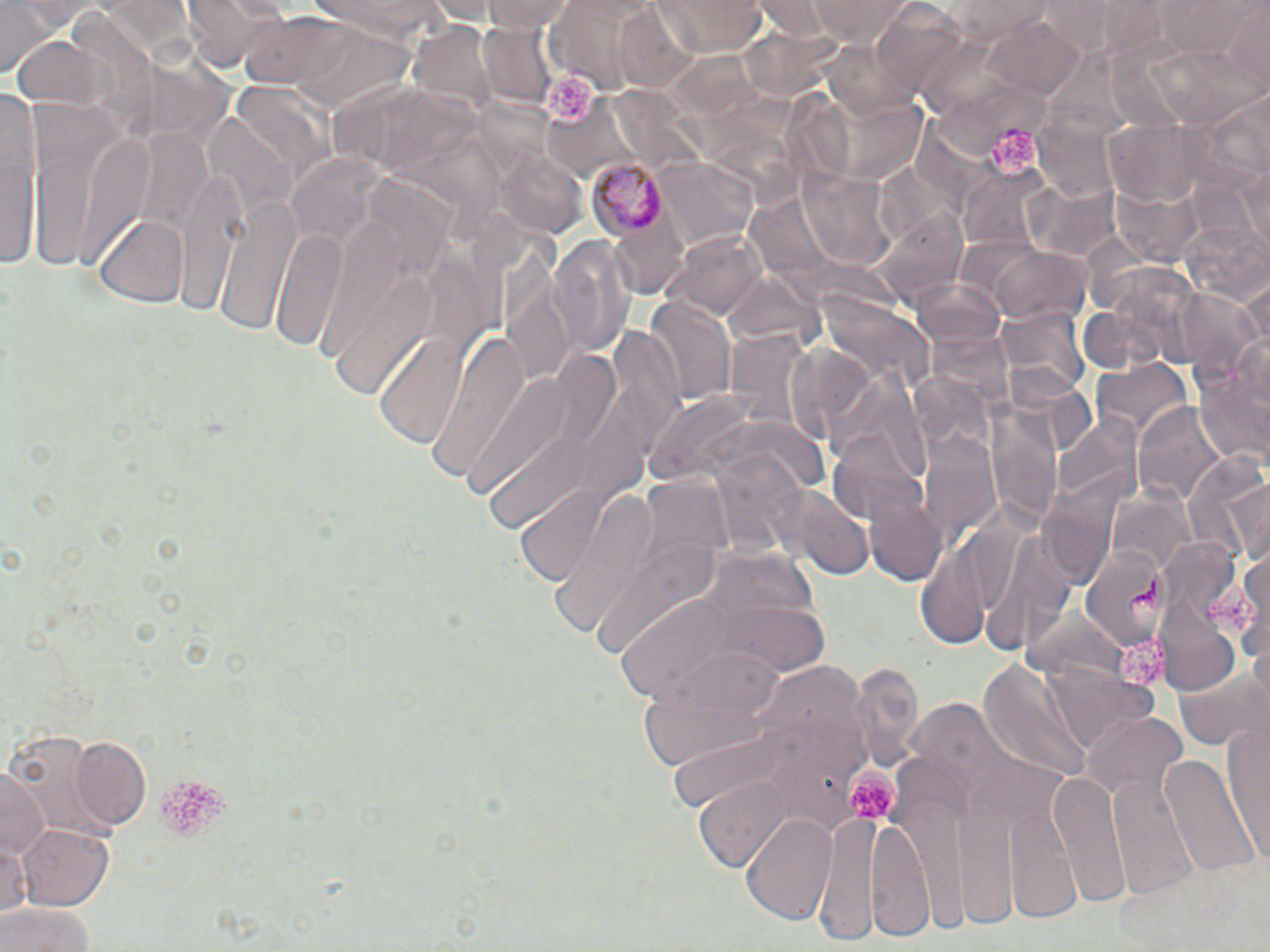

Approximate bounding boxes as (x1,y1)-(x2,y2) corner pairs in pixels. Uninfected red blood cell locations: (1,0)-(58,79), (183,0)-(278,73), (309,0)-(449,43), (482,0)-(578,34), (655,0)-(768,55), (806,0)-(914,44), (952,2)-(1060,41), (1158,2)-(1262,57), (988,16)-(1089,101), (478,19)-(558,109), (0,89)-(41,276), (212,195)-(298,335), (95,213)-(190,306), (670,230)-(770,320), (269,231)-(348,352), (552,235)-(636,359), (990,247)-(1090,329), (644,297)-(734,406), (999,303)-(1090,404), (427,329)-(531,481), (372,332)-(471,450), (1193,340)-(1270,471), (1091,356)-(1192,444), (1136,404)-(1228,507), (1183,453)-(1270,563), (866,487)-(949,587), (537,488)-(661,634), (1234,542)-(1270,672), (633,641)-(787,778), (1172,662)-(1268,750), (1220,712)-(1270,861), (1084,713)-(1188,805), (71,739)-(151,830), (1162,751)-(1263,880), (0,766)-(47,861), (1050,771)-(1129,907), (697,778)-(795,872), (813,813)-(939,945), (741,814)-(837,925), (18,823)-(116,911), (0,900)-(99,952). Platelet locations: (540,69)-(600,125), (983,125)-(1039,173), (1204,582)-(1263,637), (1114,639)-(1173,689), (844,763)-(906,819), (159,773)-(227,838). Plasmodium malariae-infected red blood cell locations: (586,160)-(670,239), (1079,548)-(1173,647). Slide-level diagnosis: Plasmodium malariae. Image is 1270×952 pixels. One field of a larger specimen. Thin blood film. 1000x magnification. Light microscopy. May-Grünwald-Giemsa-stained preparation.